Comment on the morphology of the erythrocytes.
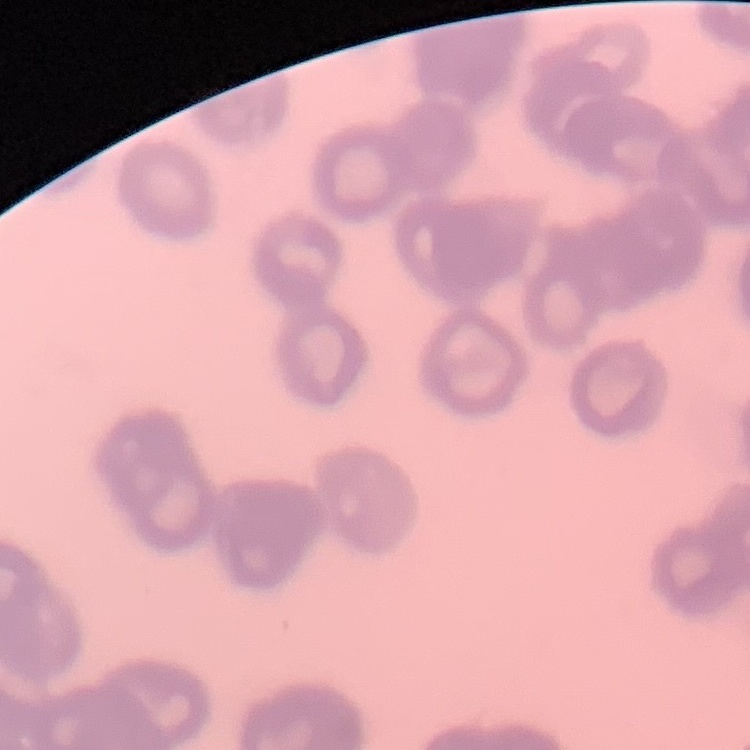
Rouleaux formation.

stain = Field's or Giemsa
image type = square crop of a larger photomicrograph
preparation = thin blood film